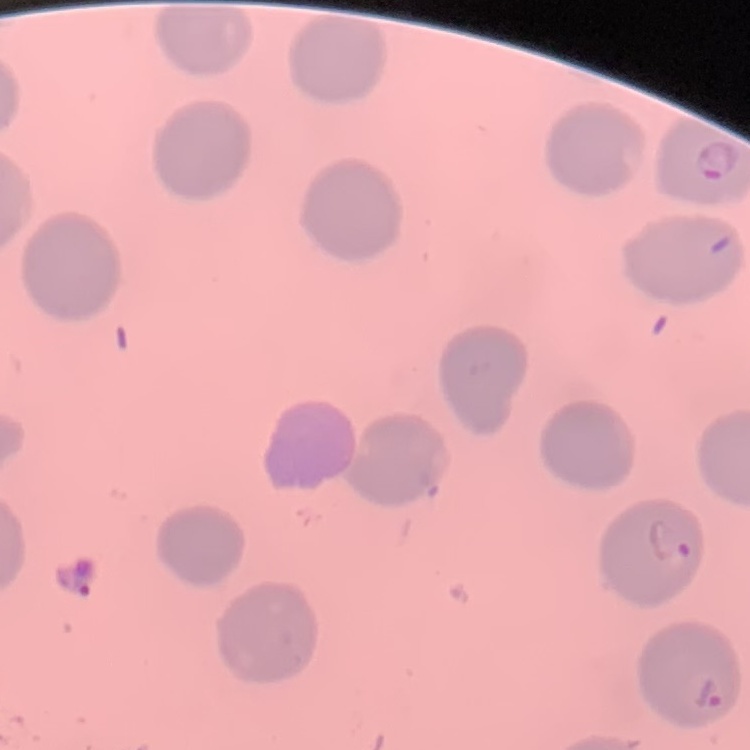

red blood cell morphology = no rouleaux formation
preparation = thin blood film
image type = one tile cut from a larger photomicrograph
stain = Field's or Giemsa